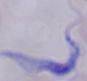
modality: photomicrograph
identification: trypanosome
magnification: 1000x